Classify the preparation.
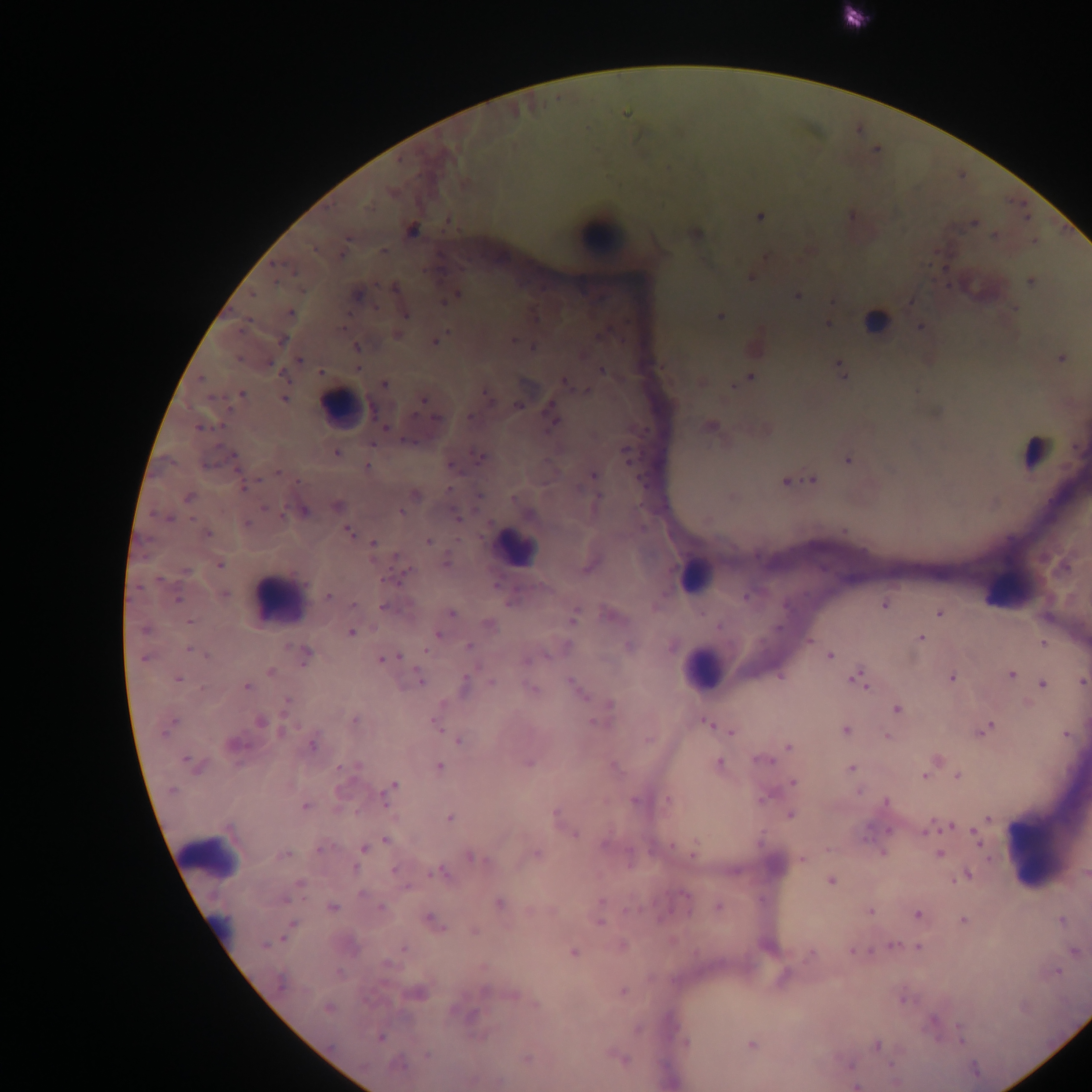

Thick blood film.

Approximate centers as (x, y) in pixels. Leukocyte locations: (601, 235), (876, 321), (340, 408), (1034, 451), (514, 547), (695, 576), (1007, 588), (278, 599), (702, 668), (1046, 853), (211, 856). Plasmodium parasite locations: (760, 217), (973, 224), (412, 230), (995, 236), (1034, 241), (383, 251), (751, 278), (1031, 282), (394, 288), (252, 294), (357, 294), (797, 295), (455, 296), (444, 301), (290, 313), (406, 314), (719, 316), (827, 324), (920, 327), (397, 335), (282, 340), (514, 341), (435, 342), (356, 348), (533, 348), (1062, 359), (300, 362), (358, 368), (840, 369), (602, 370), (321, 372), (750, 376), (200, 379), (743, 380), (565, 383), (384, 384), (734, 386), (587, 391), (242, 394), (284, 399), (491, 400), (423, 401), (518, 405), (551, 408), (436, 417), (469, 417), (553, 423), (711, 426), (202, 428), (384, 428), (409, 441), (625, 451), (336, 453), (481, 457), (847, 459), (235, 462), (451, 466), (367, 467), (278, 472), (593, 475), (813, 480), (786, 482), (243, 487), (448, 488), (414, 495), (479, 496), (598, 496), (189, 497), (338, 505), (264, 508), (304, 511), (401, 512), (457, 515), (529, 515), (166, 519), (246, 524), (349, 532), (207, 533), (428, 541), (373, 543), (447, 563), (220, 565), (1066, 567), (186, 571), (403, 575), (225, 594), (328, 596), (746, 598), (177, 599), (885, 604), (354, 605), (384, 607), (451, 613), (939, 613), (574, 618), (190, 621), (489, 625), (719, 627), (145, 629), (352, 633), (437, 634), (921, 638), (810, 641), (1043, 643), (468, 646), (629, 646), (189, 650), (305, 653), (830, 655), (207, 656), (395, 657), (146, 659), (383, 660), (527, 660), (270, 671), (1011, 675), (780, 676), (952, 677), (858, 679), (178, 680), (421, 681), (1082, 682), (491, 683), (1043, 684), (465, 686), (247, 687), (574, 687), (531, 689), (287, 701), (610, 705), (897, 709), (355, 720), (261, 722), (171, 723), (595, 723), (707, 723), (437, 726), (985, 729), (167, 731), (283, 731), (731, 731), (845, 731), (1067, 735), (888, 737), (459, 742), (234, 744), (313, 744), (789, 747), (763, 760), (190, 762), (528, 763), (719, 763), (356, 766), (439, 766), (613, 766), (851, 769), (924, 776), (958, 776), (794, 783), (395, 785), (172, 791), (858, 792), (389, 793), (764, 798), (668, 799), (384, 800), (634, 801), (886, 802), (305, 807), (555, 812), (790, 815), (450, 818), (988, 818), (950, 826), (889, 830), (925, 831), (975, 833), (575, 834), (978, 839), (386, 840), (605, 844), (672, 845), (321, 848), (364, 848), (882, 853), (285, 854), (536, 854), (692, 854), (940, 854), (471, 857), (802, 859), (354, 869), (395, 871), (439, 872), (1085, 873), (966, 875), (831, 882), (300, 883), (361, 893), (684, 895), (284, 899), (602, 901), (499, 904), (332, 907), (718, 907), (381, 908), (870, 911), (917, 914), (432, 921), (964, 921), (1061, 921), (600, 922), (292, 924), (475, 931), (264, 944), (893, 945), (623, 946), (918, 948), (403, 949), (853, 951), (1074, 952), (574, 953), (811, 954), (387, 964), (1058, 971), (280, 982), (485, 991), (622, 991), (416, 993), (513, 995), (904, 1000), (535, 1004), (329, 1009), (933, 1020), (638, 1030), (961, 1035), (380, 1038), (685, 1042), (752, 1044), (877, 1045), (427, 1055), (525, 1058), (623, 1058), (398, 1065), (891, 1065), (855, 1086). Single field of view. Mobile-phone photograph taken through the microscope. Sample from Ghana. Image is 1092×1092 pixels.